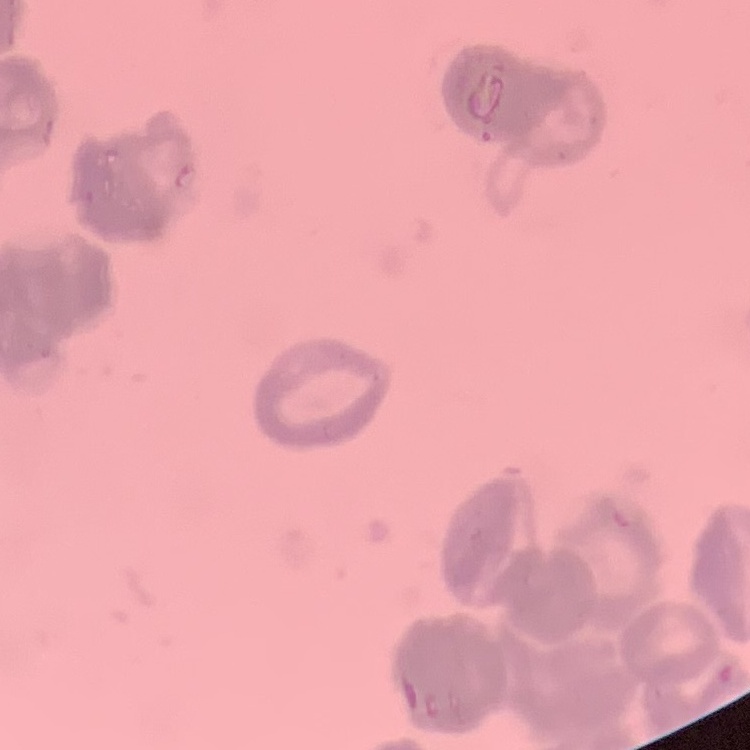
The erythrocytes exhibit rouleaux formation. One tile cut from a larger photomicrograph. Stained with either Field's or Giemsa. Thin peripheral smear.